Comment on the morphology of the red blood cells.
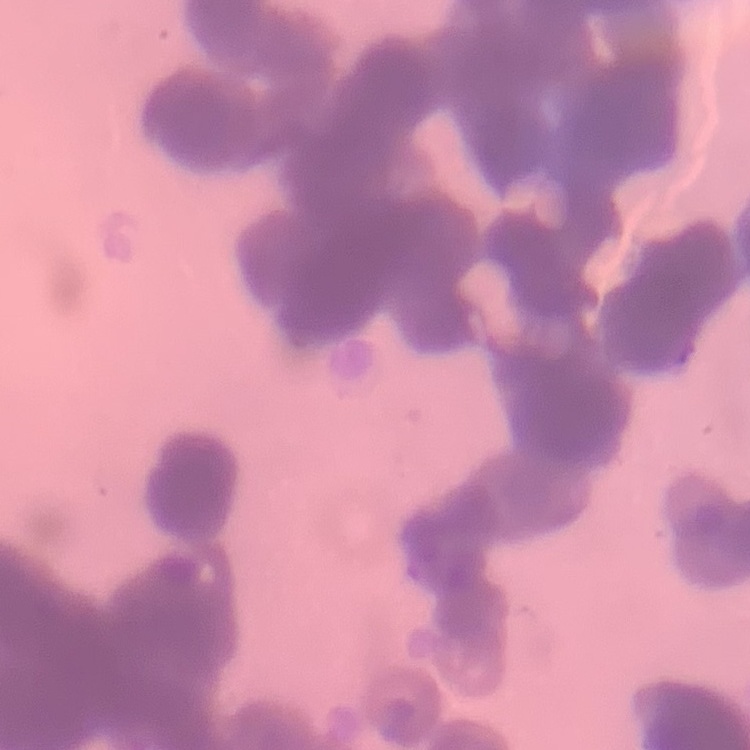

They show rouleaux formation.

Thin blood film. One tile cut from a larger photomicrograph. Stained with either Field's or Giemsa.